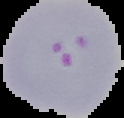
Summary:
  - Malaria status: parasitized
  - Preparation: thin blood smear
  - Image size: 124×118 pixels
  - Image type: cell region segmented out of the field of view; surrounding area masked to black